Classify this cell by malaria status.
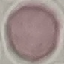
Uninfected.

Summary:
  - Stain: Giemsa
  - Preparation: thin blood film
  - Capture: smartphone through the microscope eyepiece
  - Image type: cell patch, automatically extracted from a larger field of view and resized to 64 × 64 pixels